Give the position of every Plasmodium parasite visible.
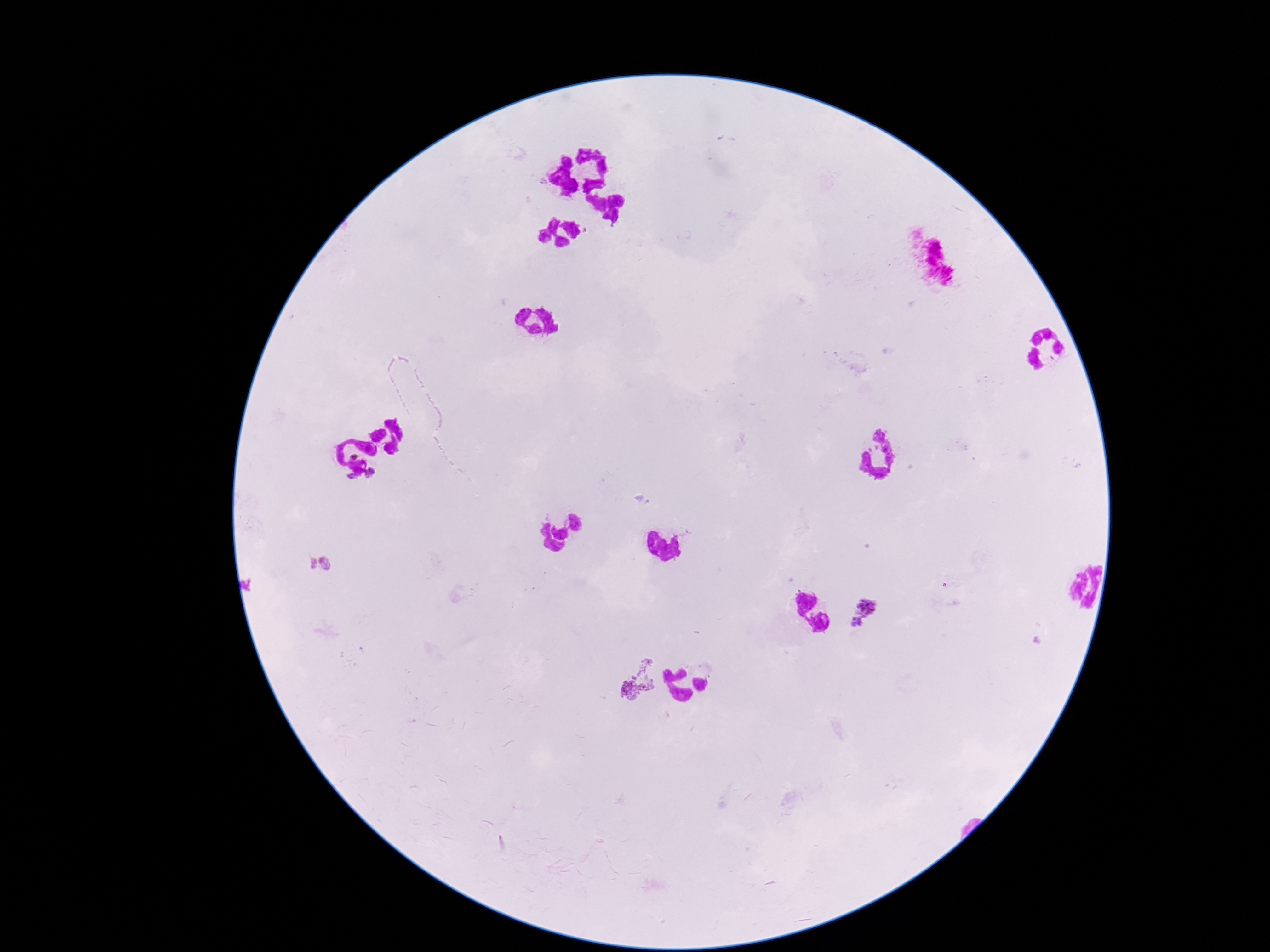

Approximate centers as {x, y} in pixels.
Plasmodium parasites: {316, 565}, {865, 614}, {629, 677}.

{
  "preparation": "thick peripheral-blood smear",
  "patient_malaria_status": "positive",
  "field_of_view": "one from this slide",
  "capture": "smartphone camera through the microscope eyepiece",
  "magnification": "100x",
  "image_size": "1270×952 pixels",
  "stain": "Giemsa"
}